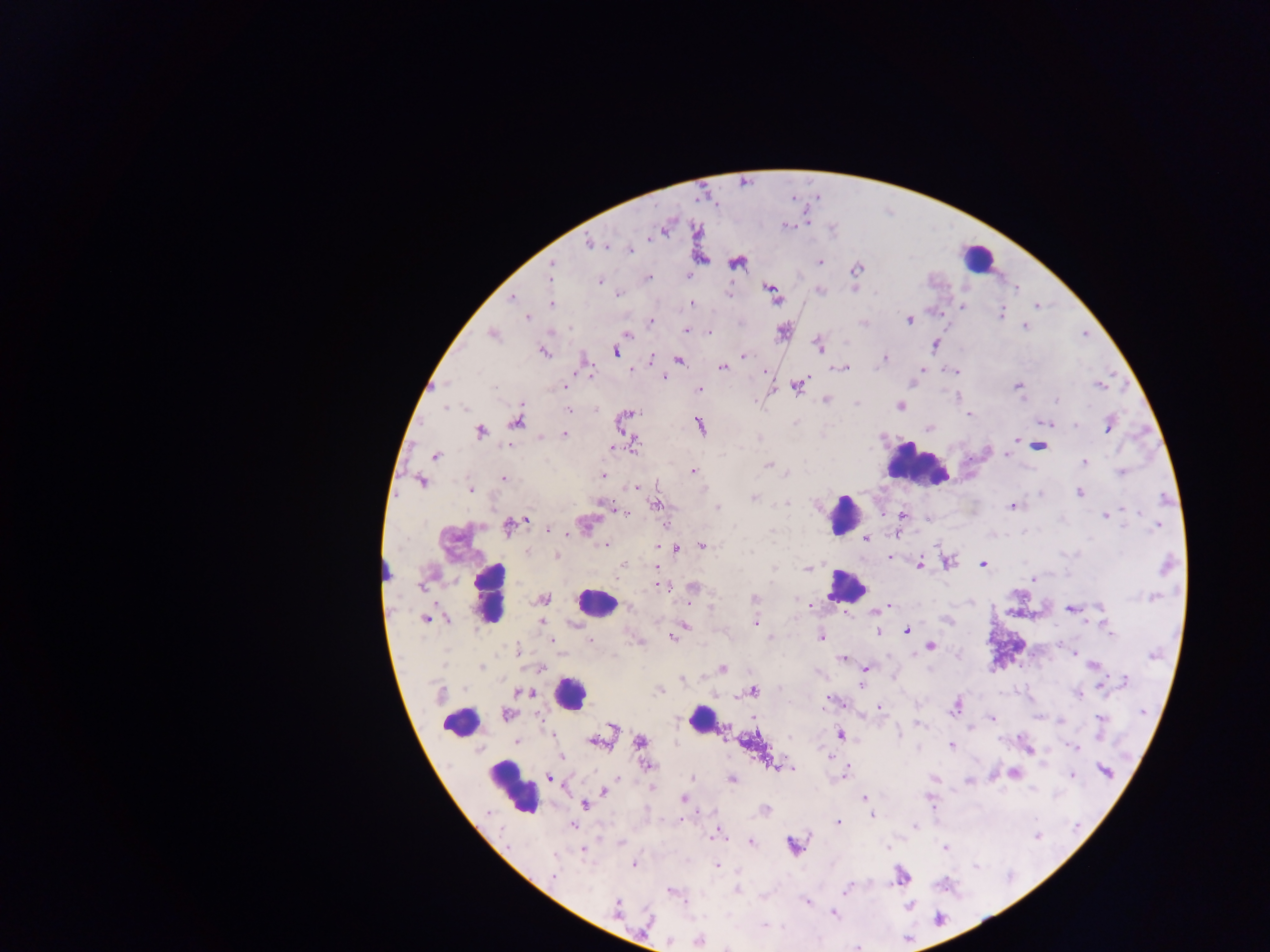
Approximate centers as (x, y) in pixels. Plasmodium parasite locations: (697, 199), (650, 237), (588, 245), (608, 249), (629, 251), (706, 260), (818, 262), (551, 263), (734, 264), (649, 276), (687, 278), (600, 282), (1016, 288), (769, 290), (728, 294), (773, 294), (618, 297), (510, 298), (550, 304), (693, 304), (1036, 305), (963, 306), (1002, 313), (526, 316), (651, 321), (909, 321), (863, 322), (1025, 325), (687, 329), (709, 331), (1086, 334), (626, 336), (936, 345), (819, 348), (543, 352), (615, 354), (744, 354), (653, 357), (885, 357), (679, 361), (721, 369), (846, 369), (924, 370), (632, 371), (954, 371), (765, 372), (663, 376), (912, 383), (567, 384), (1100, 385), (494, 386), (797, 387), (1019, 387), (700, 389), (825, 399), (1057, 400), (899, 406), (567, 408), (969, 415), (627, 417), (621, 419), (516, 423), (1109, 423), (700, 425), (1050, 426), (1075, 426), (928, 430), (1107, 430), (480, 432), (564, 435), (1017, 438), (541, 441), (508, 446), (613, 447), (635, 447), (1039, 447), (1002, 455), (434, 456), (1006, 456), (1084, 463), (768, 464), (692, 471), (1120, 472), (786, 473), (603, 475), (503, 479), (423, 482), (636, 487), (471, 488), (1079, 492), (1040, 495), (754, 498), (786, 503), (654, 504), (1012, 505), (717, 507), (1124, 509), (1135, 511), (902, 513), (626, 514), (1104, 515), (528, 519), (926, 521), (666, 525), (1159, 525), (507, 526), (1125, 528), (548, 529), (586, 529), (584, 535), (866, 538), (605, 544), (655, 546), (702, 547), (678, 550), (751, 551), (556, 556), (892, 557), (948, 563), (982, 565), (654, 567), (807, 567), (920, 567), (389, 572), (422, 586), (670, 588), (1157, 598), (544, 599), (892, 606), (1100, 607), (710, 608), (1068, 610), (874, 614), (426, 619), (448, 619), (946, 620), (543, 622), (574, 623), (755, 623), (686, 624), (877, 630), (1108, 630), (908, 632), (674, 635), (771, 637), (822, 638), (672, 639), (590, 640), (551, 641), (930, 646), (1074, 655), (843, 657), (480, 665), (1093, 665), (541, 666), (723, 670), (866, 670), (683, 680), (1126, 680), (1100, 685), (861, 686), (752, 692), (524, 694), (1080, 697), (829, 698), (878, 708), (954, 709), (951, 712), (1140, 713), (507, 714), (539, 717), (990, 719), (1059, 722), (918, 724), (610, 727), (971, 728), (753, 730), (550, 734), (840, 734), (899, 734), (551, 737), (517, 741), (1001, 741), (598, 743), (639, 743), (591, 744), (951, 745), (1073, 747), (1027, 751), (828, 757), (774, 765), (648, 766), (1105, 772), (846, 773), (1014, 774), (1073, 774), (550, 777), (693, 778), (732, 781), (967, 782), (653, 788), (1031, 789), (603, 791), (863, 797), (684, 799), (584, 805), (871, 816), (838, 821), (680, 822), (574, 826), (916, 827), (715, 836), (1035, 837), (709, 838), (751, 842), (619, 843), (790, 844), (887, 846), (794, 848), (944, 848), (583, 854), (718, 866), (634, 867), (553, 878), (903, 879), (845, 889), (737, 891), (671, 892), (803, 900), (908, 905), (832, 913), (938, 918), (764, 925), (698, 941), (857, 946). Leukocyte locations: (977, 261), (916, 466), (843, 515), (845, 589), (489, 596), (595, 606), (579, 695), (700, 717), (455, 722), (514, 794). Single field of view. Thick blood film. Image is 1270×952 pixels. Collected in Ghana. Photographed through a microscope with a mobile-phone camera.